Report the malaria status of this cell.
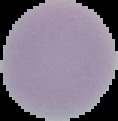

Uninfected.

image size = 118×121 pixels
preparation = thin blood film
image type = cell region segmented out of the field of view; surrounding area masked to black